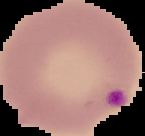

Summary:
  - Image type: cell region segmented out of the field of view; surrounding area masked to black
  - Image size: 145×136 pixels
  - Result: malaria parasites identified
  - Preparation: thin blood smear